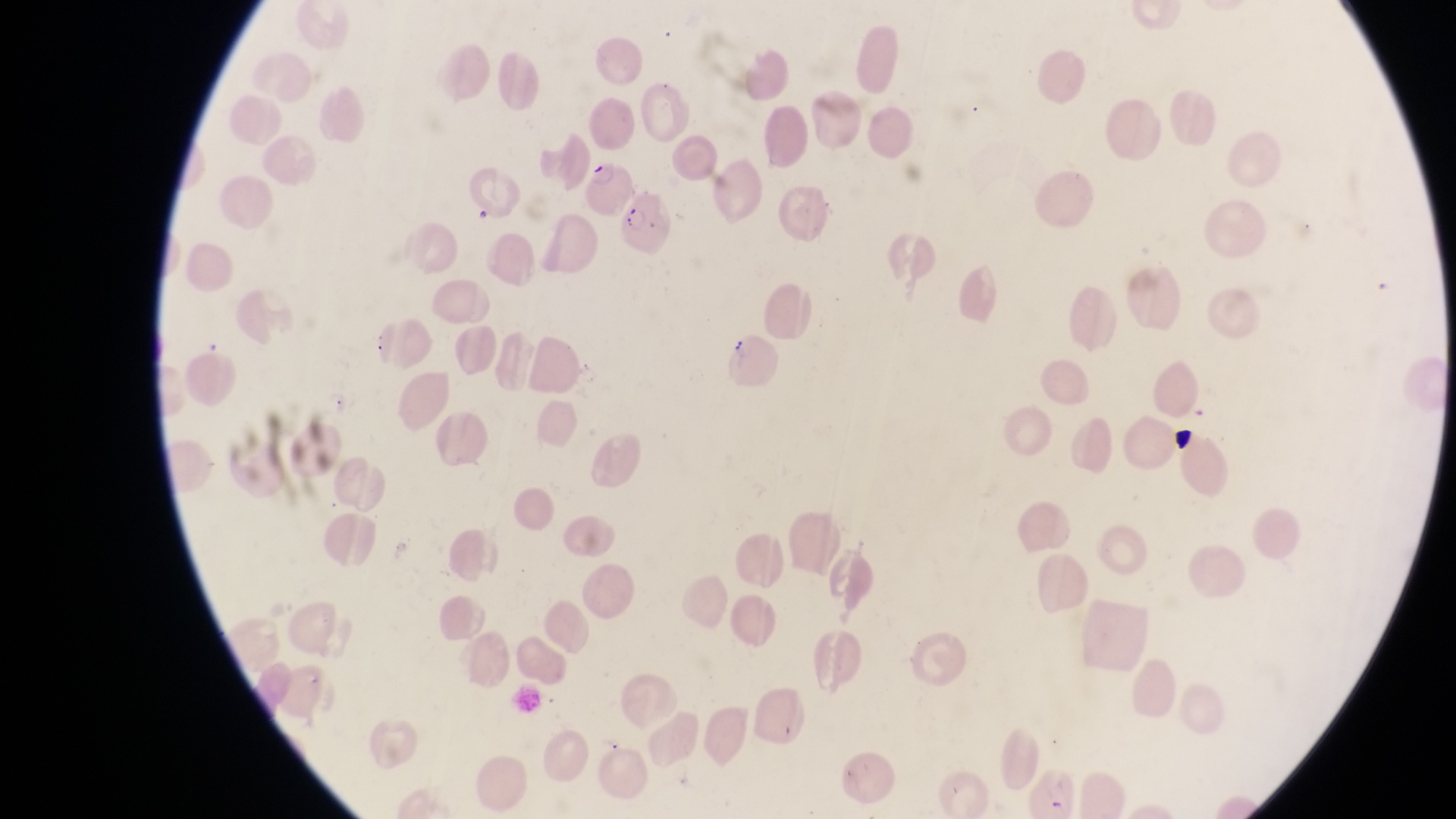
Approximate bounding boxes as (left, top, right, bottom) in pixels. Artifact (platelet-like body, stain precipitate, or debris) locations: (1169, 425, 1198, 455). Parasitised red blood cell locations: (587, 155, 629, 215), (618, 196, 676, 259). One field of view. Captured by a smartphone held over the eyepiece of an Olympus CX-23 microscope. At a magnification of 1000x. Collected in Uganda. Image is 1456×819 pixels. Thin blood smear.